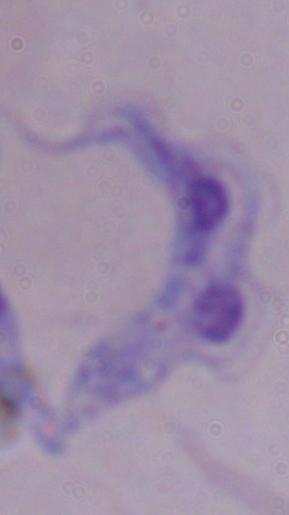

modality = micrograph
identification = trypanosome
magnification = 1000x